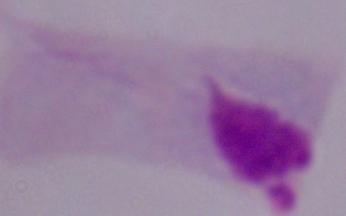

modality: photomicrograph
magnification: 1000x
identification: trichomonad